Assess the morphology of the erythrocytes.
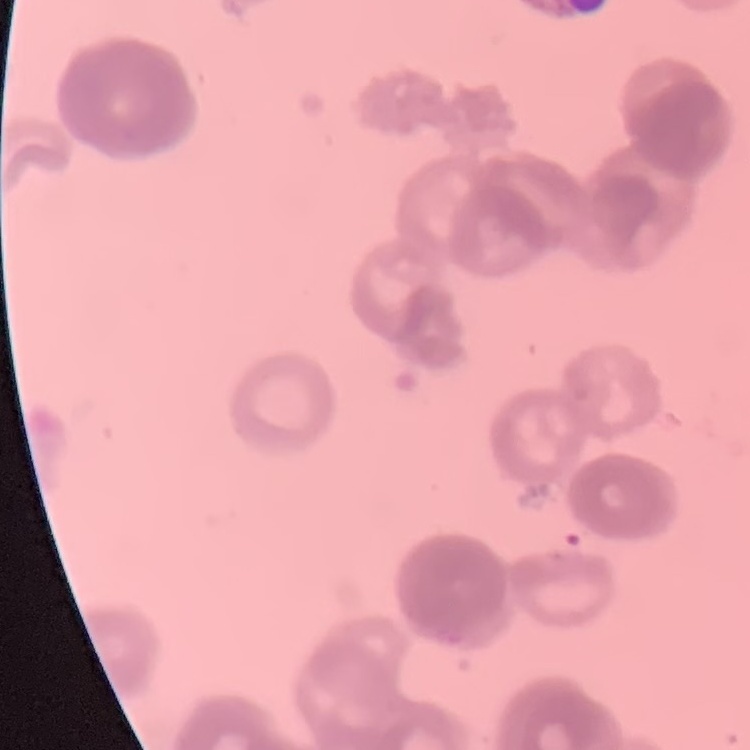
Rouleaux formation.

Square crop of a larger photomicrograph. Field's or Giemsa stain. Thin blood film.